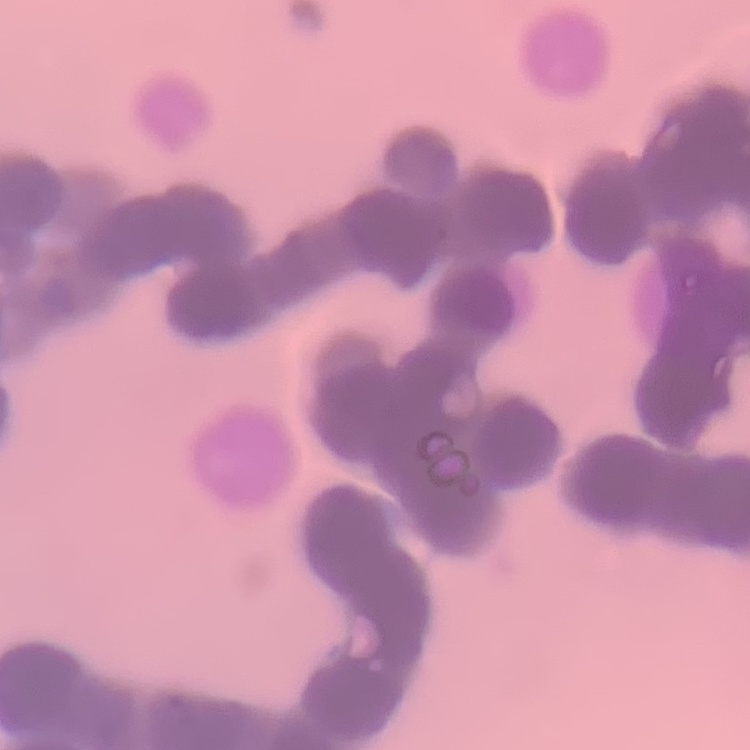

Summary:
  - Erythrocyte morphology: rouleaux formation
  - Preparation: thin blood film
  - Image type: one tile cut from a larger photomicrograph
  - Stain: Field's or Giemsa